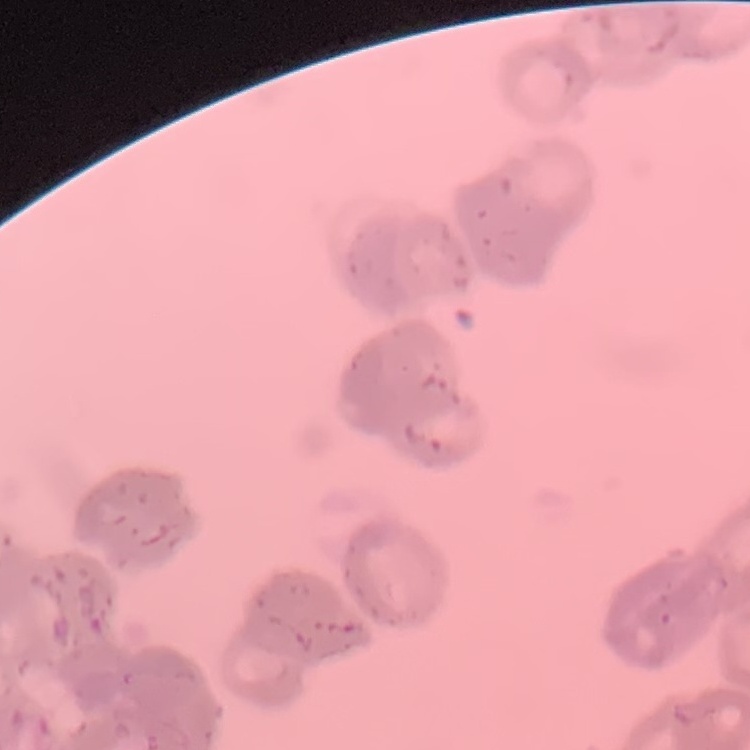

The red blood cells exhibit rouleaux formation. Thin blood smear. Square crop of a larger photomicrograph. Stained with either Field's or Giemsa.